Locate every uninfected red blood cell.
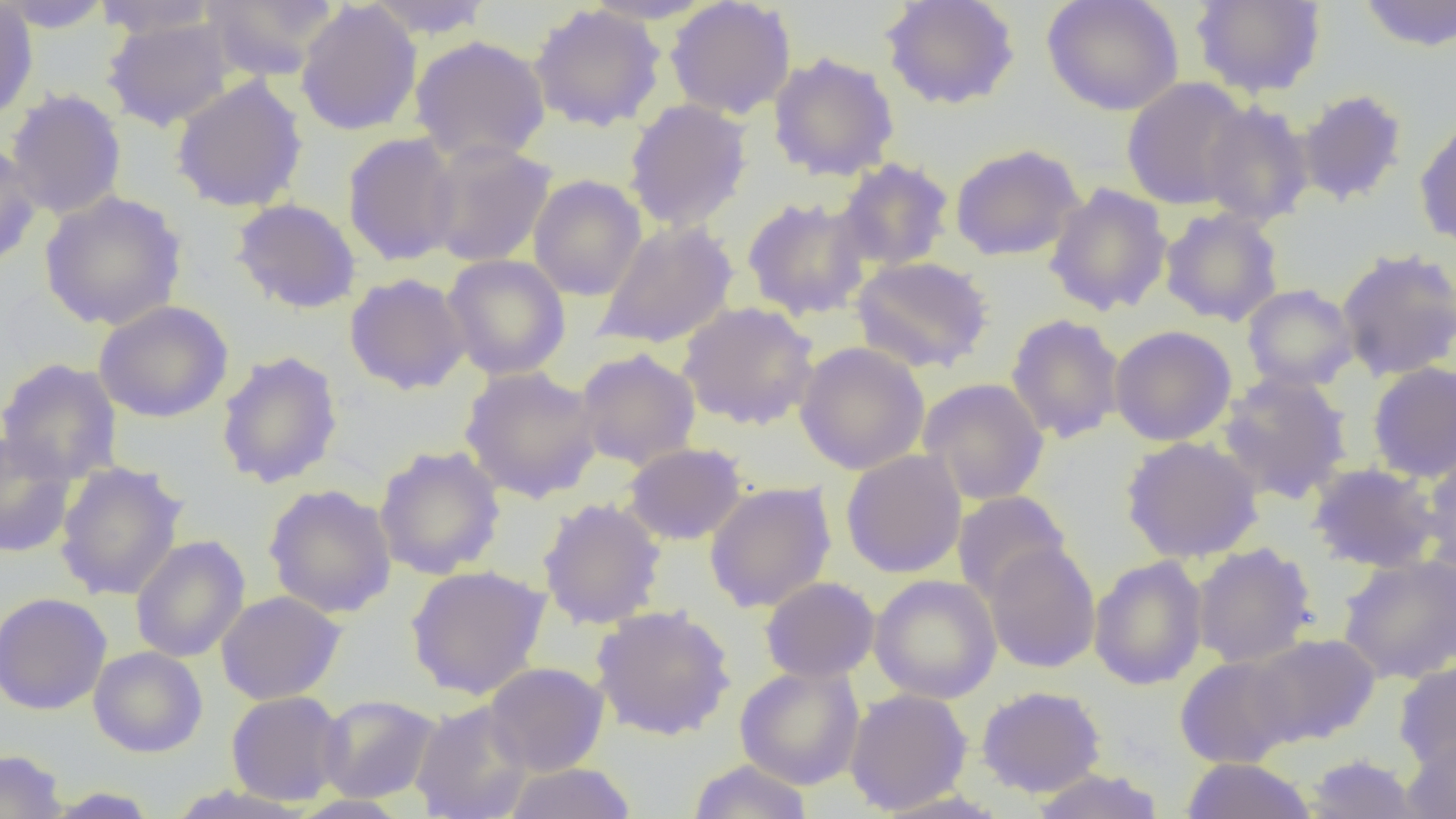

Approximate bounding boxes as (x1, y1, x2, y2) in pixels.
Uninfected red blood cells: (0, 0, 114, 33), (201, 0, 341, 81), (363, 0, 495, 39), (579, 0, 718, 25), (881, 0, 1021, 111), (1042, 0, 1184, 116), (1190, 0, 1327, 99), (1355, 0, 1455, 53), (0, 1, 38, 125), (92, 1, 223, 40), (295, 1, 423, 137), (665, 1, 797, 120), (528, 4, 667, 132), (101, 16, 239, 132), (410, 35, 550, 164), (767, 52, 900, 182), (170, 75, 308, 213), (1121, 77, 1254, 210), (5, 88, 127, 221), (1296, 89, 1409, 207), (623, 98, 753, 232), (1199, 100, 1315, 227), (1414, 114, 1456, 251), (342, 132, 463, 267), (424, 140, 557, 268), (0, 142, 42, 270), (949, 143, 1085, 262), (836, 158, 955, 272), (528, 175, 647, 301), (1044, 183, 1172, 317), (39, 190, 187, 331), (742, 196, 873, 320), (231, 198, 361, 314), (1159, 207, 1284, 327), (594, 219, 738, 350), (1335, 247, 1456, 382), (441, 254, 571, 381), (851, 256, 995, 374), (345, 273, 471, 395), (1241, 283, 1359, 392), (93, 300, 233, 423), (677, 301, 819, 431), (1005, 313, 1126, 444), (1109, 325, 1237, 446), (794, 342, 930, 475), (575, 347, 702, 472), (216, 350, 344, 489), (0, 358, 123, 484), (1367, 362, 1456, 482), (459, 366, 603, 503), (1217, 371, 1353, 504), (918, 377, 1050, 505), (0, 433, 79, 558), (1121, 436, 1264, 564), (623, 442, 748, 545), (373, 445, 506, 580), (1420, 448, 1456, 576), (841, 449, 967, 578), (53, 461, 188, 602), (1307, 462, 1440, 573), (703, 481, 837, 613), (263, 484, 397, 618), (951, 491, 1073, 603), (537, 497, 667, 630), (130, 535, 250, 663), (984, 542, 1102, 673), (1191, 543, 1317, 668), (1337, 553, 1456, 685), (1088, 555, 1208, 691), (406, 564, 551, 700), (869, 574, 1002, 704), (760, 576, 880, 683), (216, 590, 346, 705), (0, 592, 112, 715), (591, 604, 735, 741), (1247, 633, 1381, 747), (88, 646, 208, 758), (1174, 656, 1299, 768), (484, 662, 610, 776), (1393, 662, 1456, 773), (734, 665, 865, 790), (976, 685, 1106, 797), (844, 688, 973, 815), (226, 691, 348, 805), (317, 694, 441, 803), (411, 700, 533, 819), (1401, 734, 1456, 819), (0, 748, 68, 819), (1301, 753, 1427, 818), (1181, 757, 1317, 819), (687, 759, 815, 819), (502, 762, 637, 818), (1031, 767, 1165, 819), (38, 786, 162, 818), (871, 788, 1013, 819), (288, 795, 413, 818).

Summary:
  - Slide-level diagnosis: negative for blood parasites
  - Image size: 1456×819 pixels
  - Field of view: one of a larger specimen
  - Magnification: 1000x
  - Preparation: thin blood smear
  - Modality: optical microscopy